Assess this cell for malaria.
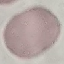
Uninfected.

stain: Giemsa
image_type: cell patch, automatically extracted from a larger field of view and resized to 64 × 64 pixels
preparation: thin blood smear
capture: smartphone through the microscope eyepiece